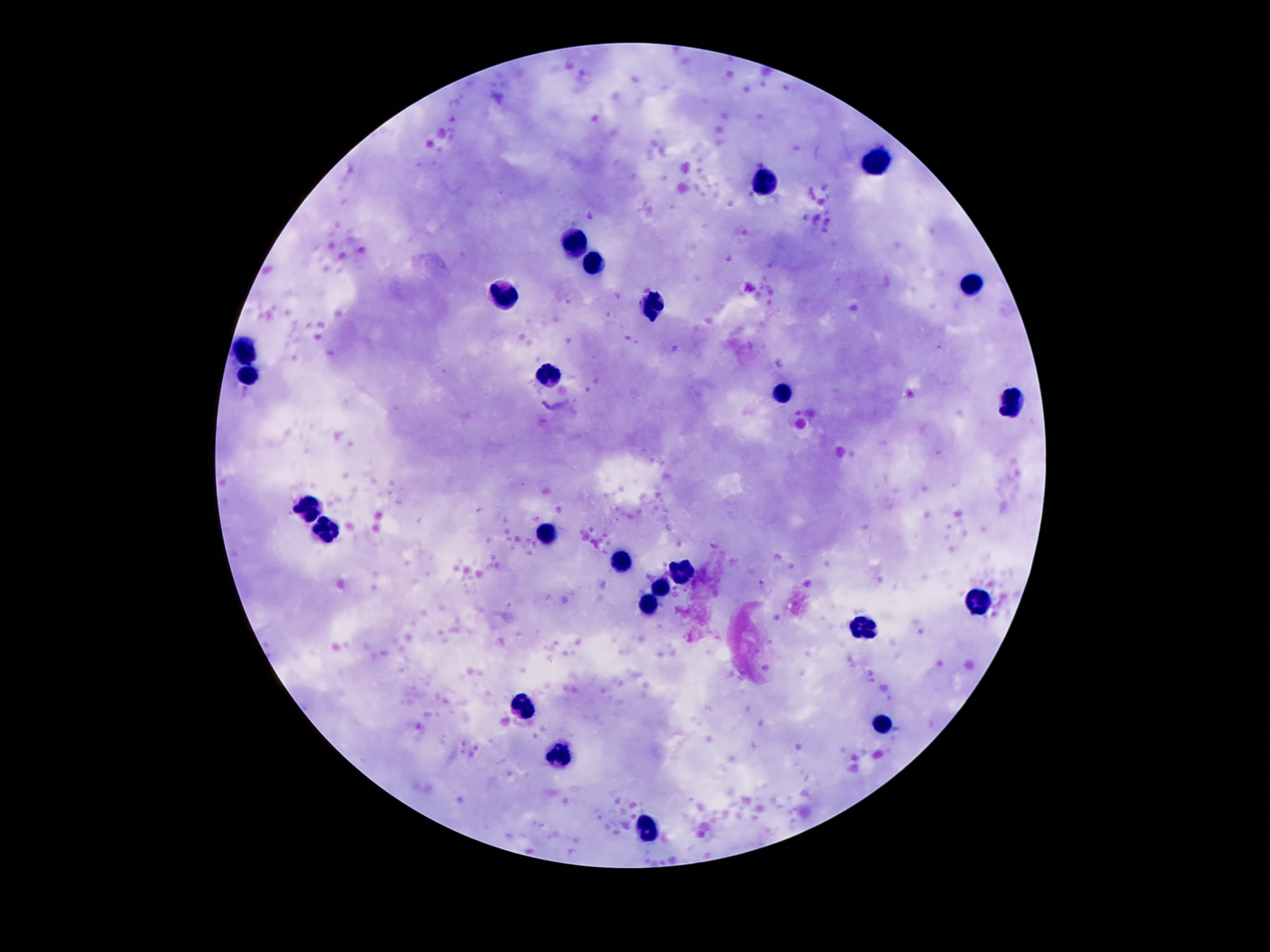

Approximate object centers, in pixels from the top-left corner.
Summary:
  - Leukocyte locations: (x=878, y=163), (x=764, y=181), (x=576, y=243), (x=596, y=265), (x=972, y=288), (x=502, y=296), (x=652, y=306), (x=252, y=348), (x=250, y=374), (x=550, y=377), (x=785, y=395), (x=1011, y=403), (x=311, y=507), (x=324, y=525), (x=548, y=535), (x=621, y=561), (x=680, y=571), (x=662, y=589), (x=977, y=602), (x=647, y=603), (x=861, y=629), (x=523, y=707), (x=883, y=722), (x=558, y=755), (x=647, y=830)
  - Capture: smartphone camera through the microscope eyepiece
  - Preparation: thick blood film
  - Stain: Giemsa
  - Field of view: single
  - Patient malaria status: uninfected
  - Image size: 1270×952 pixels
  - Magnification: 100x